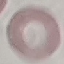

Result: negative for malaria parasites. Thin blood smear. Giemsa-stained preparation. Photographed with a smartphone camera at the microscope eyepiece. Cell patch, automatically extracted from a larger field of view and resized to 64 × 64 pixels.